Name the parasite shown.
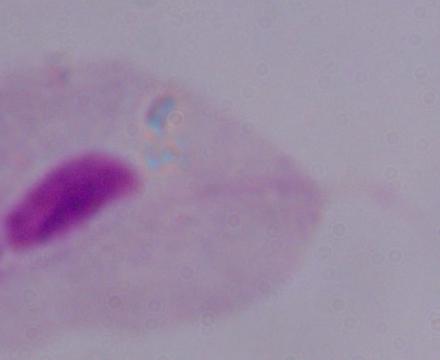
This is a trichomonad.

Summary:
  - Magnification: 1000x
  - Modality: photomicrograph